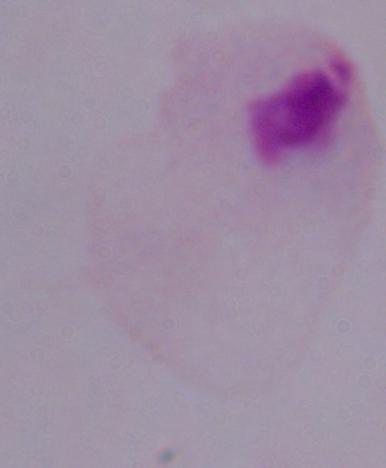 Captured at 1000x magnification. A trichomonad is shown. Photomicrograph.